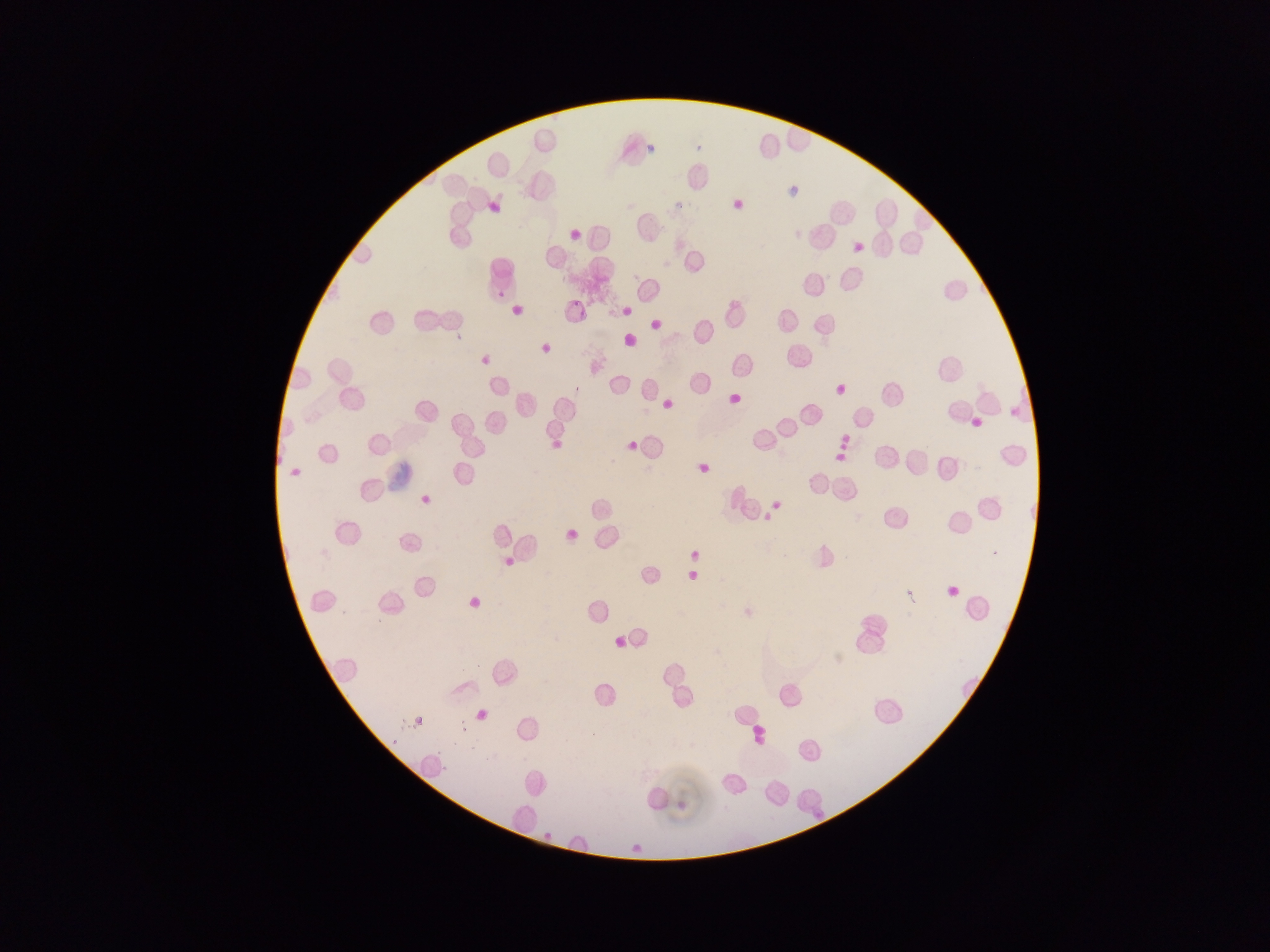

Approximate bounding boxes as [left, top, right, bottom] in pixels.
Summary:
  - Plasmodium parasite locations: [694, 143, 707, 152], [647, 144, 655, 153], [569, 295, 580, 311], [397, 718, 414, 729], [388, 736, 398, 745], [813, 810, 822, 817], [539, 825, 554, 845] | approximate [x, y] pixel centers of objects too small to bound: [463, 727]
  - Capture: mobile-phone photograph through a microscope
  - Preparation: thin blood smear
  - Image size: 1270×952 pixels
  - Field of view: single
  - Country: Ghana